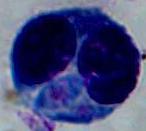

magnification = 1000x
identification = white blood cell
modality = micrograph